State the blood parasite species.
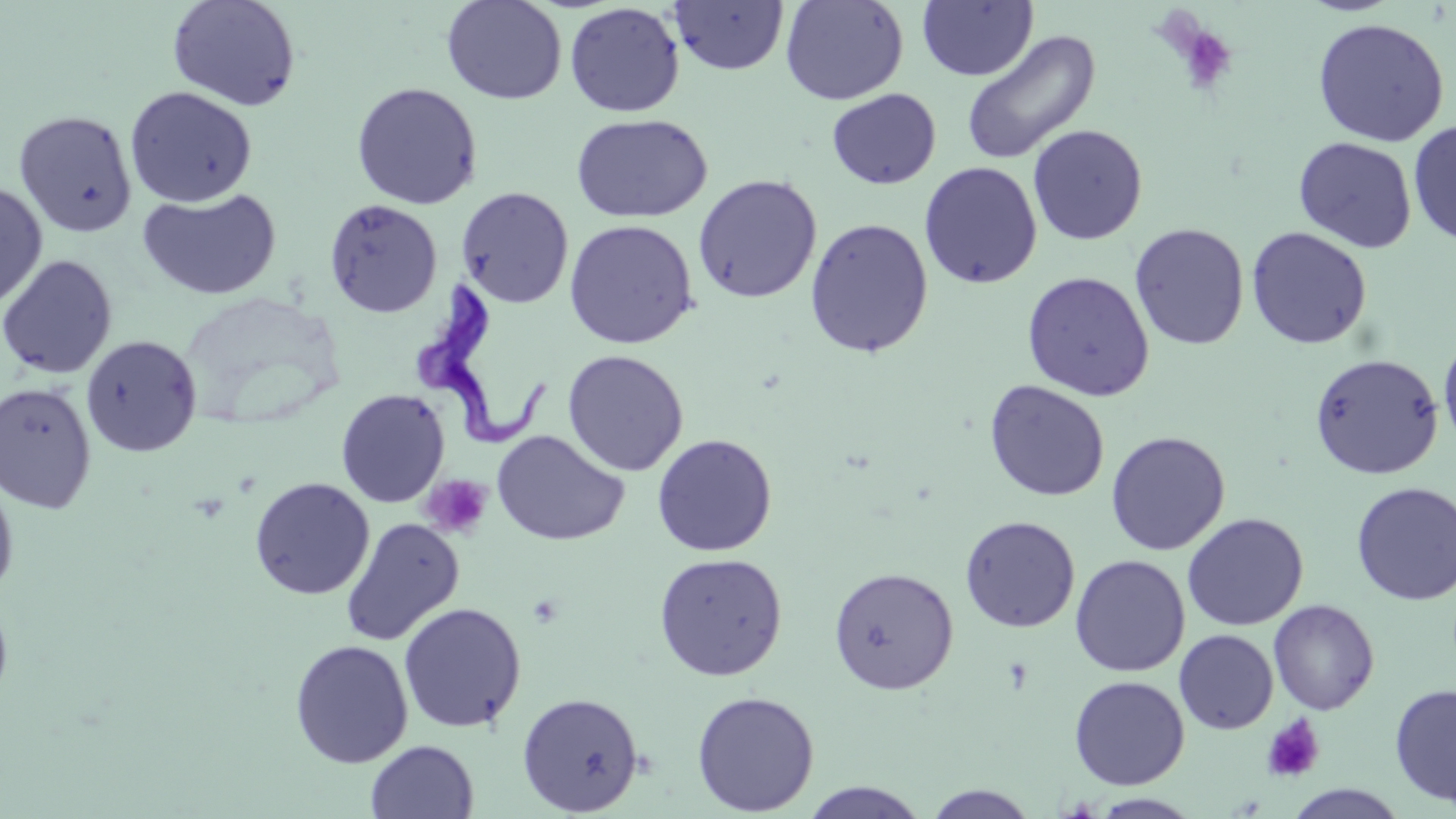
Trypanosoma brucei.

Approximate bounding boxes as named x1/y1/x2/y2 corners in pixels. Uninfected red blood cell locations: (x1=441, y1=0, x2=567, y2=105), (x1=780, y1=0, x2=908, y2=105), (x1=166, y1=1, x2=301, y2=112), (x1=669, y1=1, x2=790, y2=75), (x1=918, y1=1, x2=1037, y2=82), (x1=565, y1=2, x2=684, y2=117), (x1=1312, y1=17, x2=1450, y2=146), (x1=960, y1=30, x2=1101, y2=165), (x1=350, y1=81, x2=483, y2=209), (x1=125, y1=86, x2=257, y2=207), (x1=826, y1=88, x2=942, y2=190), (x1=14, y1=110, x2=138, y2=238), (x1=570, y1=114, x2=712, y2=223), (x1=1408, y1=120, x2=1456, y2=248), (x1=1027, y1=124, x2=1147, y2=245), (x1=1293, y1=137, x2=1417, y2=253), (x1=919, y1=162, x2=1042, y2=289), (x1=692, y1=174, x2=822, y2=304), (x1=0, y1=181, x2=49, y2=311), (x1=456, y1=187, x2=574, y2=309), (x1=137, y1=188, x2=282, y2=301), (x1=324, y1=199, x2=443, y2=319), (x1=804, y1=217, x2=934, y2=358), (x1=563, y1=219, x2=699, y2=349), (x1=1129, y1=223, x2=1249, y2=350), (x1=1246, y1=226, x2=1372, y2=349), (x1=0, y1=254, x2=118, y2=379), (x1=1022, y1=271, x2=1155, y2=401), (x1=1439, y1=332, x2=1456, y2=454), (x1=81, y1=334, x2=202, y2=457), (x1=562, y1=350, x2=689, y2=476), (x1=1309, y1=353, x2=1444, y2=480), (x1=984, y1=380, x2=1109, y2=502), (x1=0, y1=381, x2=97, y2=514), (x1=335, y1=389, x2=450, y2=508), (x1=491, y1=430, x2=629, y2=546), (x1=1106, y1=431, x2=1230, y2=556), (x1=652, y1=433, x2=777, y2=556), (x1=0, y1=473, x2=19, y2=602), (x1=249, y1=477, x2=374, y2=600), (x1=1351, y1=481, x2=1456, y2=606), (x1=1182, y1=513, x2=1308, y2=631), (x1=960, y1=515, x2=1080, y2=632), (x1=340, y1=517, x2=464, y2=647), (x1=653, y1=552, x2=788, y2=681), (x1=1070, y1=555, x2=1190, y2=677), (x1=828, y1=566, x2=959, y2=695), (x1=0, y1=591, x2=14, y2=716), (x1=1268, y1=599, x2=1379, y2=715), (x1=398, y1=602, x2=527, y2=733), (x1=1174, y1=629, x2=1278, y2=734), (x1=290, y1=639, x2=413, y2=768), (x1=1068, y1=675, x2=1190, y2=790), (x1=1389, y1=683, x2=1456, y2=807), (x1=691, y1=690, x2=819, y2=816), (x1=517, y1=692, x2=643, y2=816), (x1=365, y1=740, x2=479, y2=818), (x1=797, y1=782, x2=932, y2=818), (x1=1285, y1=784, x2=1408, y2=818), (x1=922, y1=785, x2=1040, y2=818), (x1=1088, y1=793, x2=1204, y2=818). Platelet locations: (x1=1173, y1=24, x2=1238, y2=95), (x1=421, y1=474, x2=493, y2=539), (x1=1261, y1=714, x2=1326, y2=784). Trypanosoma brucei locations: (x1=415, y1=276, x2=546, y2=453). Image is 1456×819 pixels. One field of a larger specimen. Thin blood smear. Light microscopy. Captured at 1000x magnification. May-Grünwald-Giemsa stain.